Report the malaria status of this cell.
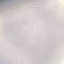
It is uninfected.

capture = smartphone camera at the microscope eyepiece
stain = Giemsa
image type = automatically extracted cell patch, resized to 64 × 64 pixels
preparation = thin smear